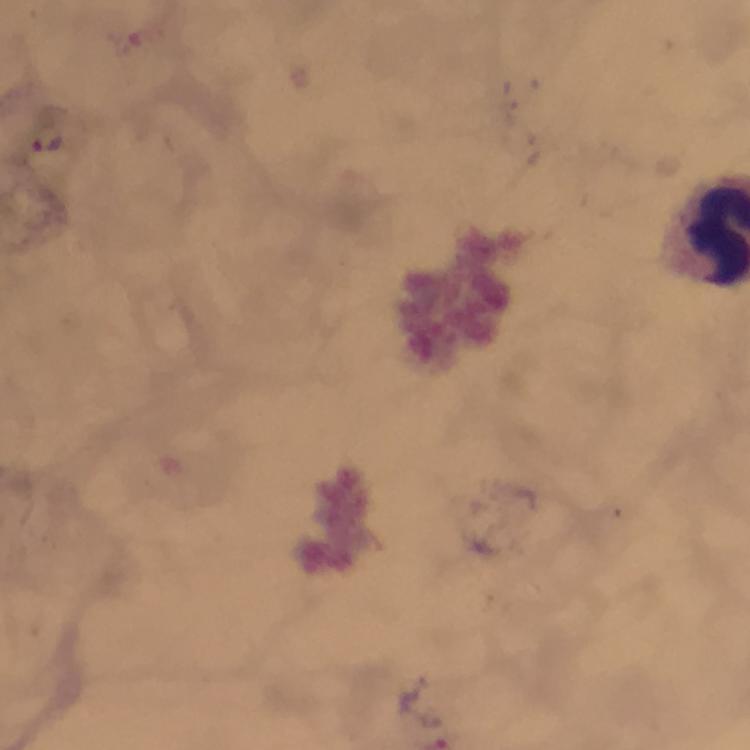 Approximate object centers, in pixels from the top-left corner. Plasmodium parasite locations: (x=48, y=145). Image is 750×750 pixels. Cropped region of a single field of view. Smartphone photograph taken through a microscope. From a malaria diagnostic workup. Thick blood film. 100x magnification. Giemsa-stained preparation. Immersion oil was used.